Name the parasite shown.
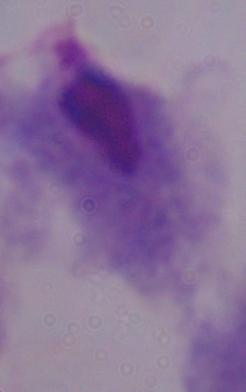
A trichomonad.

modality = micrograph
magnification = 1000x